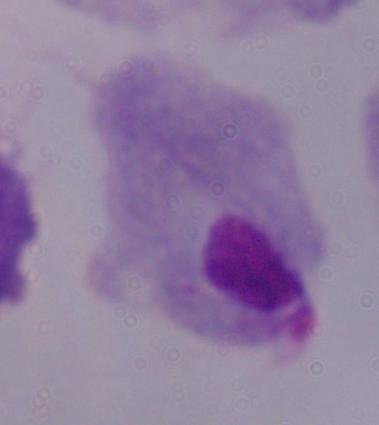
modality = micrograph
identification = trichomonad
magnification = 1000x